Assess this cell for malaria.
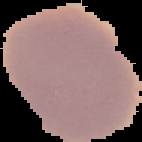
Uninfected.

Summary:
  - Image type: cell region segmented out of the field of view; surrounding area masked to black
  - Preparation: thin blood smear
  - Image size: 142×142 pixels